Identify the parasite.
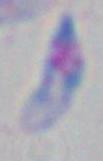
This is Toxoplasma gondii.

Captured at 1000x magnification. Micrograph.